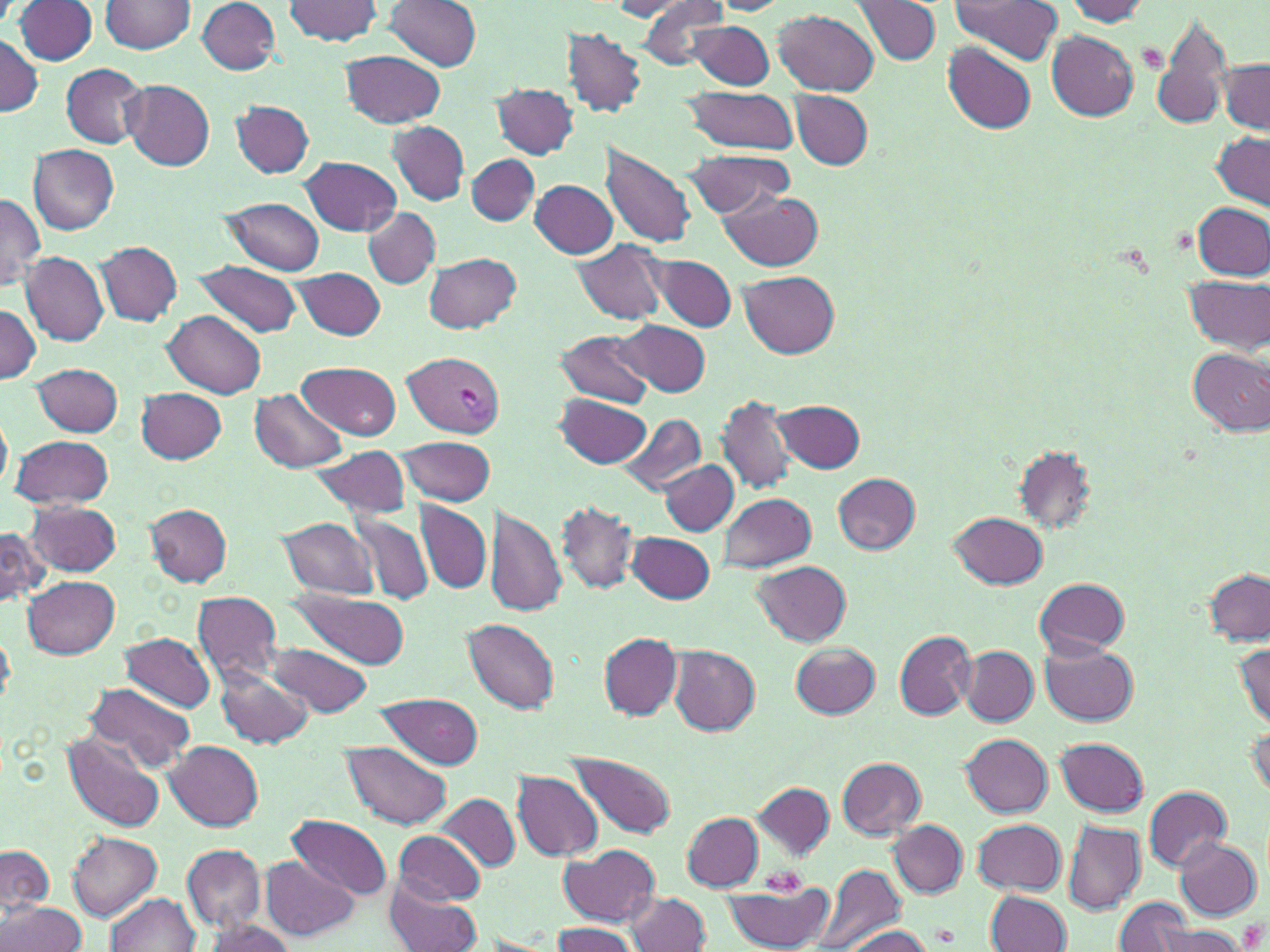 Approximate bounding boxes as named x1/y1/x2/y2 corners in pixels. Uninfected red blood cell locations: (x1=101, y1=0, x2=195, y2=55), (x1=197, y1=0, x2=280, y2=74), (x1=283, y1=0, x2=383, y2=45), (x1=386, y1=0, x2=482, y2=71), (x1=633, y1=0, x2=734, y2=71), (x1=950, y1=0, x2=1062, y2=64), (x1=1062, y1=0, x2=1151, y2=24), (x1=15, y1=1, x2=99, y2=65), (x1=609, y1=1, x2=703, y2=20), (x1=851, y1=1, x2=941, y2=66), (x1=9, y1=3, x2=187, y2=60), (x1=775, y1=9, x2=878, y2=96), (x1=1152, y1=15, x2=1231, y2=131), (x1=689, y1=18, x2=775, y2=90), (x1=563, y1=28, x2=647, y2=117), (x1=1045, y1=30, x2=1138, y2=119), (x1=0, y1=33, x2=40, y2=116), (x1=942, y1=42, x2=1036, y2=133), (x1=340, y1=50, x2=446, y2=128), (x1=1217, y1=59, x2=1269, y2=134), (x1=61, y1=63, x2=148, y2=147), (x1=122, y1=80, x2=215, y2=169), (x1=492, y1=83, x2=579, y2=159), (x1=680, y1=86, x2=803, y2=157), (x1=791, y1=91, x2=873, y2=169), (x1=231, y1=101, x2=313, y2=177), (x1=388, y1=122, x2=469, y2=205), (x1=1211, y1=130, x2=1269, y2=210), (x1=29, y1=144, x2=118, y2=234), (x1=600, y1=144, x2=699, y2=249), (x1=678, y1=148, x2=793, y2=218), (x1=468, y1=155, x2=540, y2=225), (x1=301, y1=156, x2=401, y2=236), (x1=530, y1=179, x2=619, y2=259), (x1=717, y1=190, x2=826, y2=271), (x1=0, y1=194, x2=44, y2=292), (x1=222, y1=198, x2=324, y2=274), (x1=1194, y1=202, x2=1268, y2=281), (x1=364, y1=208, x2=440, y2=288), (x1=572, y1=240, x2=668, y2=326), (x1=95, y1=241, x2=181, y2=324), (x1=21, y1=251, x2=108, y2=345), (x1=425, y1=252, x2=522, y2=334), (x1=647, y1=253, x2=738, y2=332), (x1=194, y1=260, x2=303, y2=337), (x1=295, y1=267, x2=386, y2=339), (x1=738, y1=270, x2=838, y2=357), (x1=1183, y1=275, x2=1269, y2=354), (x1=0, y1=302, x2=40, y2=385), (x1=165, y1=310, x2=266, y2=397), (x1=615, y1=319, x2=710, y2=397), (x1=555, y1=329, x2=654, y2=408), (x1=1186, y1=347, x2=1270, y2=437), (x1=298, y1=360, x2=401, y2=440), (x1=33, y1=363, x2=122, y2=437), (x1=136, y1=387, x2=227, y2=463), (x1=250, y1=389, x2=346, y2=472), (x1=555, y1=394, x2=650, y2=467), (x1=717, y1=394, x2=797, y2=496), (x1=774, y1=400, x2=866, y2=473), (x1=615, y1=410, x2=704, y2=497), (x1=0, y1=413, x2=11, y2=494), (x1=12, y1=434, x2=113, y2=507), (x1=397, y1=435, x2=495, y2=506), (x1=306, y1=445, x2=412, y2=518), (x1=1011, y1=445, x2=1097, y2=533), (x1=662, y1=460, x2=738, y2=533), (x1=835, y1=473, x2=920, y2=554), (x1=718, y1=492, x2=816, y2=573), (x1=27, y1=501, x2=121, y2=575), (x1=416, y1=501, x2=491, y2=592), (x1=557, y1=501, x2=638, y2=594), (x1=485, y1=503, x2=566, y2=618), (x1=147, y1=504, x2=233, y2=585), (x1=350, y1=510, x2=434, y2=606), (x1=948, y1=510, x2=1047, y2=588), (x1=277, y1=517, x2=379, y2=600), (x1=0, y1=525, x2=48, y2=605), (x1=627, y1=531, x2=715, y2=604), (x1=754, y1=561, x2=852, y2=644), (x1=1202, y1=569, x2=1269, y2=645), (x1=22, y1=575, x2=121, y2=657), (x1=1034, y1=578, x2=1130, y2=656), (x1=289, y1=591, x2=411, y2=669), (x1=191, y1=592, x2=284, y2=683), (x1=464, y1=619, x2=560, y2=712), (x1=1, y1=626, x2=15, y2=708), (x1=893, y1=630, x2=977, y2=720), (x1=120, y1=632, x2=215, y2=712), (x1=599, y1=632, x2=683, y2=719), (x1=1231, y1=638, x2=1270, y2=729), (x1=264, y1=640, x2=372, y2=717), (x1=791, y1=641, x2=881, y2=719), (x1=1040, y1=643, x2=1136, y2=726), (x1=670, y1=646, x2=760, y2=734), (x1=962, y1=648, x2=1038, y2=725), (x1=212, y1=663, x2=313, y2=749), (x1=85, y1=682, x2=195, y2=773), (x1=374, y1=691, x2=486, y2=767), (x1=1246, y1=718, x2=1270, y2=803), (x1=62, y1=732, x2=166, y2=832), (x1=961, y1=733, x2=1052, y2=815), (x1=1055, y1=737, x2=1148, y2=816), (x1=166, y1=742, x2=262, y2=829), (x1=342, y1=742, x2=453, y2=829), (x1=568, y1=755, x2=676, y2=838), (x1=838, y1=757, x2=925, y2=839), (x1=513, y1=772, x2=604, y2=860), (x1=753, y1=781, x2=834, y2=858), (x1=1143, y1=785, x2=1230, y2=870), (x1=436, y1=794, x2=520, y2=871), (x1=681, y1=812, x2=765, y2=889), (x1=288, y1=815, x2=394, y2=901), (x1=973, y1=819, x2=1066, y2=895), (x1=1063, y1=820, x2=1145, y2=914), (x1=889, y1=821, x2=968, y2=895), (x1=394, y1=831, x2=485, y2=905), (x1=69, y1=832, x2=161, y2=919), (x1=1174, y1=837, x2=1261, y2=919), (x1=0, y1=844, x2=53, y2=918), (x1=183, y1=844, x2=266, y2=931), (x1=559, y1=844, x2=659, y2=927), (x1=259, y1=856, x2=358, y2=941), (x1=808, y1=863, x2=907, y2=952), (x1=719, y1=877, x2=836, y2=952), (x1=383, y1=878, x2=481, y2=951), (x1=985, y1=890, x2=1070, y2=951), (x1=624, y1=892, x2=710, y2=951), (x1=106, y1=893, x2=199, y2=952), (x1=1112, y1=897, x2=1205, y2=952), (x1=1, y1=901, x2=86, y2=951), (x1=202, y1=919, x2=295, y2=951), (x1=548, y1=922, x2=639, y2=952), (x1=836, y1=924, x2=941, y2=952), (x1=1148, y1=925, x2=1246, y2=952). Plasmodium vivax-infected red blood cell locations: (x1=403, y1=352, x2=502, y2=437). Platelet locations: (x1=762, y1=868, x2=805, y2=896). Slide-level diagnosis: Plasmodium vivax. Thin blood smear. 1000x magnification. May-Grünwald-Giemsa stain. One field of a larger specimen. Light microscopy. Image is 1270×952 pixels.